Report the malaria status of this cell.
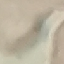

It is uninfected.

Summary:
  - Stain: Giemsa
  - Preparation: thin smear
  - Image type: automatically extracted cell patch, resized to 64 × 64 pixels
  - Capture: smartphone through the microscope eyepiece